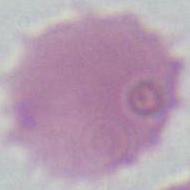

Summary:
  - Modality: micrograph
  - Magnification: 1000x
  - Identification: erythrocyte